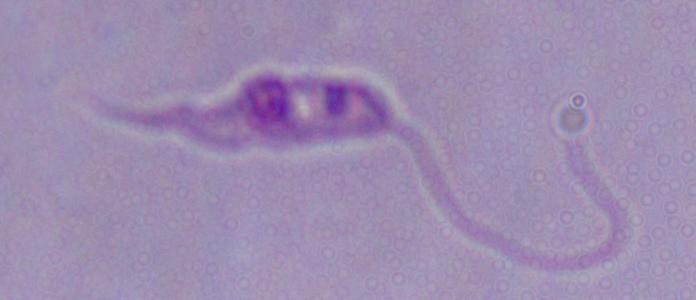 A Leishmania parasite is seen. Photomicrograph. 1000x magnification.